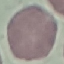
Summary:
  - Malaria status: uninfected
  - Image type: cell patch, automatically extracted from a larger field of view and resized to 64 × 64 pixels
  - Capture: smartphone through the microscope eyepiece
  - Stain: Giemsa
  - Preparation: thin blood smear